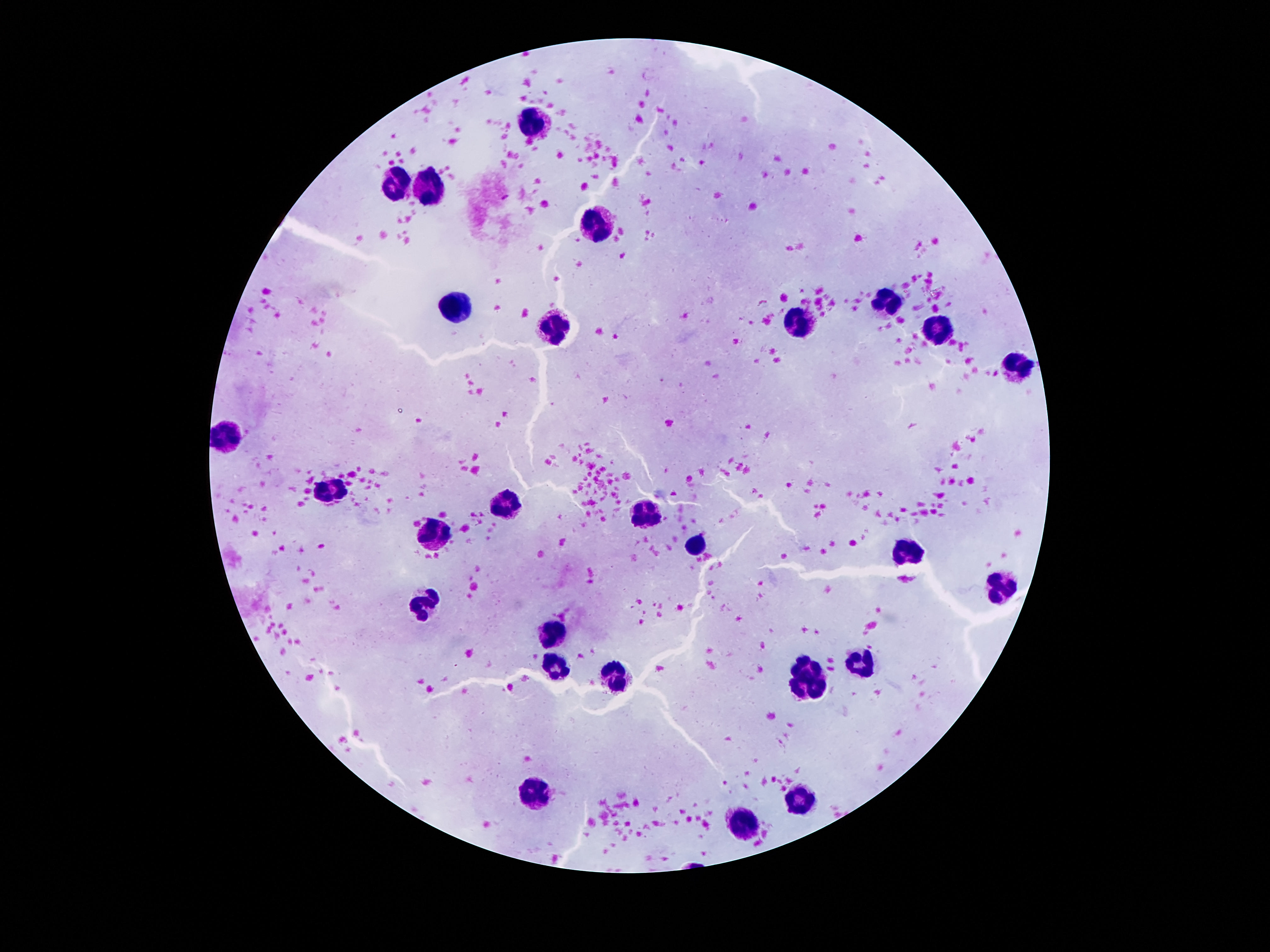
Approximate centers as {x, y} in pixels.
Summary:
  - Leukocyte locations: {535, 124}, {396, 184}, {431, 190}, {599, 225}, {455, 303}, {882, 303}, {797, 325}, {550, 327}, {934, 334}, {1021, 364}, {232, 434}, {331, 490}, {506, 504}, {647, 512}, {433, 539}, {698, 545}, {906, 552}, {999, 586}, {428, 600}, {554, 632}, {868, 660}, {557, 667}, {808, 667}, {612, 679}, {796, 687}, {820, 690}, {535, 794}, {797, 797}, {747, 825}
  - Capture: smartphone camera through the microscope eyepiece
  - Patient malaria status: negative
  - Magnification: 100x
  - Image size: 1270×952 pixels
  - Stain: Giemsa
  - Preparation: thick peripheral-blood smear
  - Field of view: single